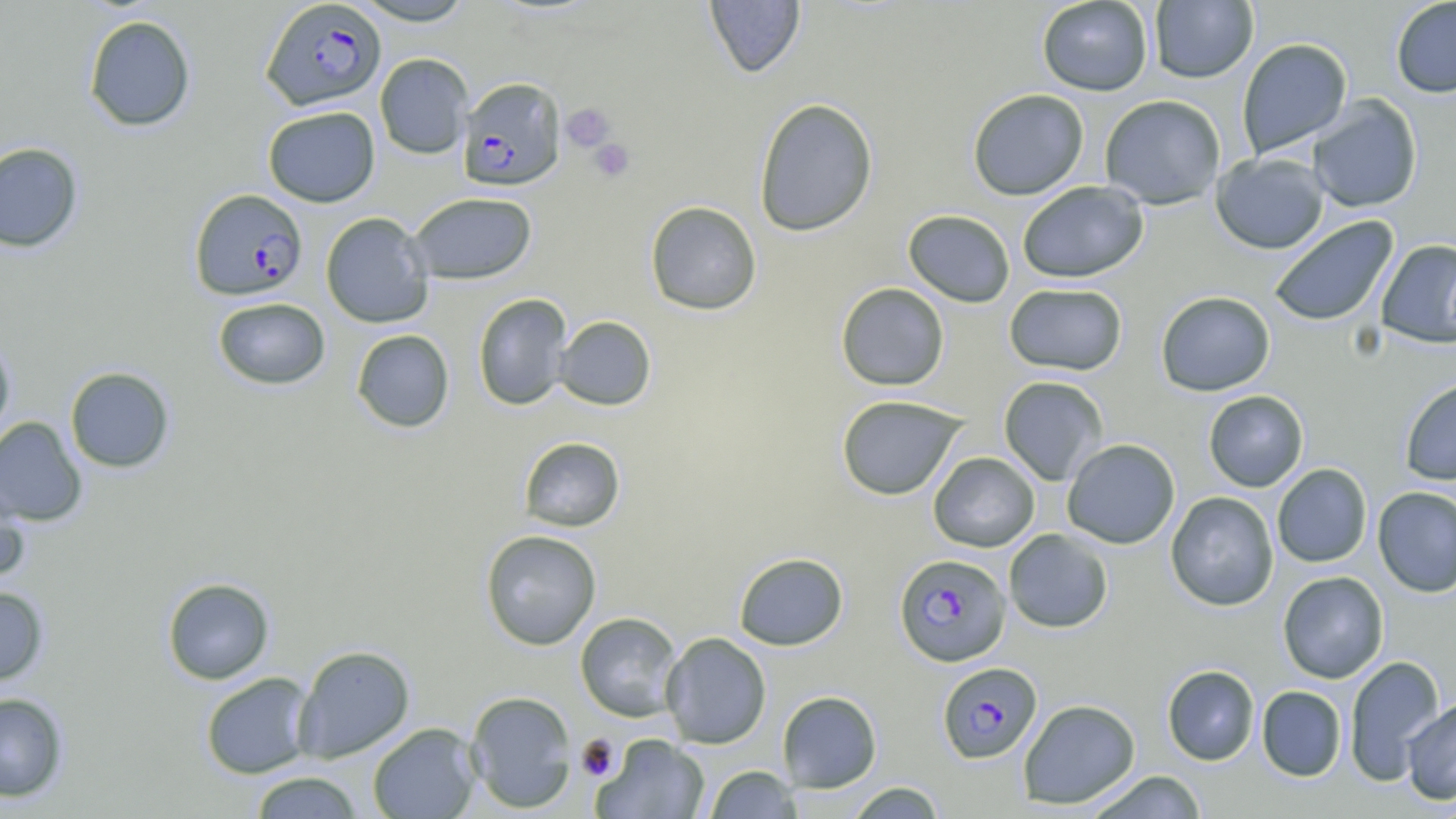

Summary:
  - Coordinate format: approximate bounding boxes as (x1,y1)-(x2,y2) corner pairs in pixels
  - Uninfected red blood cell locations: (351,0)-(478,26), (1036,0)-(1154,95), (1149,0)-(1259,83), (1390,0)-(1456,98), (704,1)-(806,78), (83,14)-(196,132), (1236,38)-(1353,158), (375,53)-(473,159), (967,88)-(1089,200), (1099,94)-(1226,209), (1306,96)-(1423,213), (753,97)-(878,237), (263,106)-(380,207), (0,142)-(84,252), (1211,152)-(1330,254), (1016,181)-(1149,284), (406,192)-(538,285), (645,201)-(762,316), (903,209)-(1016,307), (320,212)-(434,328), (1268,216)-(1399,327), (1375,239)-(1456,347), (835,282)-(950,391), (1004,283)-(1128,376), (1155,290)-(1275,396), (472,293)-(572,411), (212,297)-(331,390), (553,315)-(657,411), (351,329)-(454,433), (0,335)-(16,444), (64,367)-(176,473), (998,376)-(1109,485), (1399,377)-(1456,486), (1203,390)-(1308,492), (835,394)-(969,500), (0,417)-(88,527), (518,436)-(625,532), (1061,438)-(1180,549), (928,452)-(1040,552), (1271,463)-(1372,567), (0,475)-(31,586), (1372,486)-(1456,598), (1165,491)-(1279,611), (1003,528)-(1114,633), (480,529)-(602,650), (734,552)-(848,651), (1277,571)-(1389,683), (162,577)-(275,685), (0,586)-(49,685), (575,612)-(683,722), (660,632)-(772,748), (293,645)-(415,762), (1344,654)-(1445,784), (1162,664)-(1260,765), (200,672)-(316,779), (1256,686)-(1347,781), (777,690)-(882,792), (464,691)-(577,812), (0,692)-(69,801), (1401,697)-(1456,805), (1017,699)-(1140,809), (368,723)-(481,819), (593,734)-(710,818), (704,765)-(801,818), (1084,770)-(1208,818), (249,771)-(364,818), (844,782)-(946,818)
  - Platelet locations: (561,103)-(616,152), (588,139)-(635,182), (576,735)-(620,780)
  - Plasmodium falciparum-infected red blood cell locations: (261,0)-(387,111), (457,76)-(566,191), (190,188)-(308,301), (894,553)-(1011,667), (937,662)-(1042,763)
  - Slide-level diagnosis: Plasmodium falciparum
  - Magnification: 1000x
  - Field of view: single
  - Stain: May-Grünwald-Giemsa
  - Modality: optical microscopy
  - Preparation: thin blood smear
  - Image size: 1456×819 pixels